Look for parasitized red blood cells.
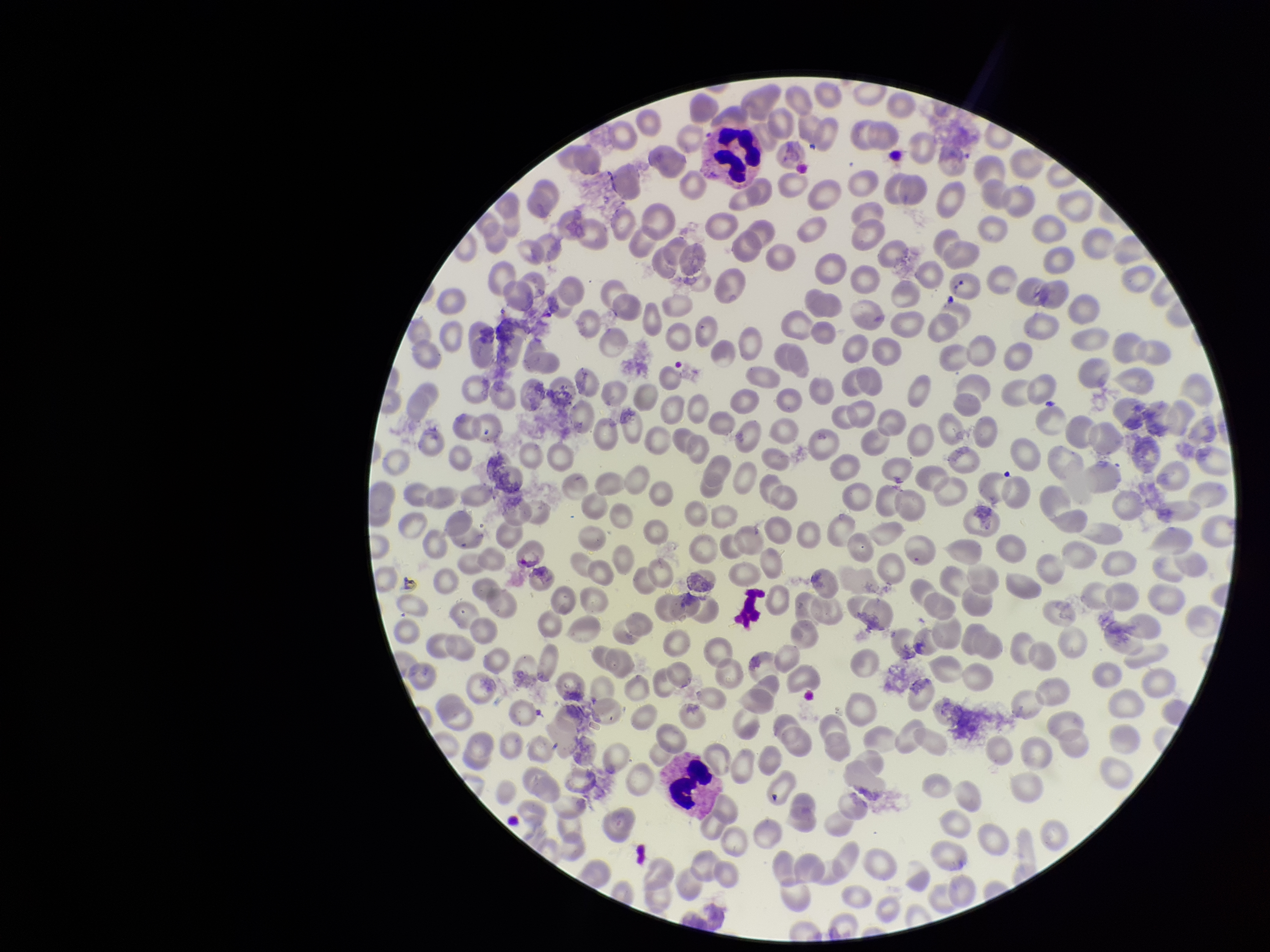

None detected.

Summary:
  - Stain: Giemsa
  - Parasitized red blood cell count: 0
  - Field of view: single
  - Image size: 1270×952 pixels
  - Preparation: thin blood smear
  - Capture: smartphone photograph through the microscope eyepiece
  - Patient malaria status: negative
  - Red blood cell count: 278